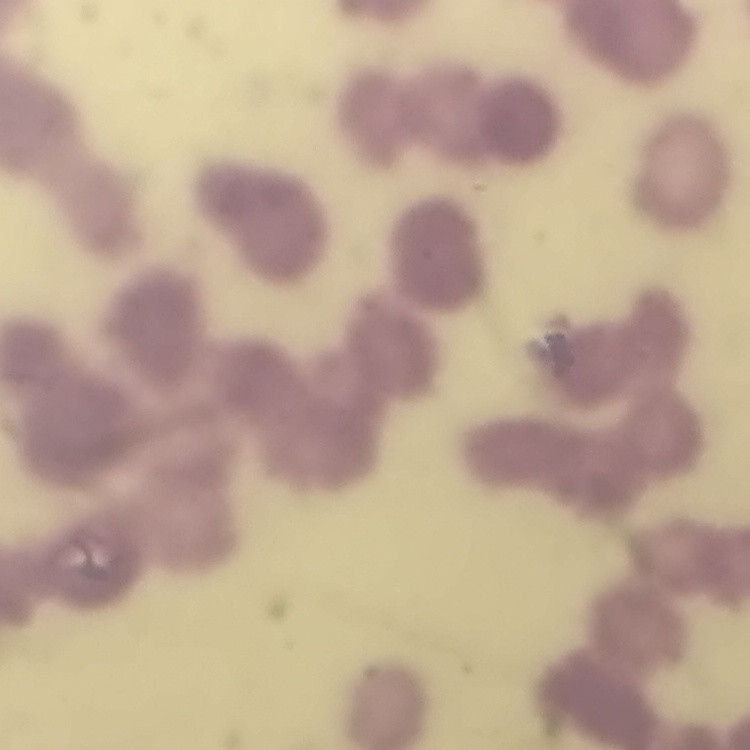

The erythrocytes show rouleaux formation. One tile cut from a larger photomicrograph. Thin peripheral smear. Field's or Giemsa stain.